Assess this cell for malaria.
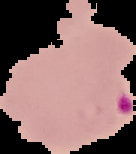
It is parasitized.

Segmented cell region on a black background. From a thin blood smear. Image is 136×154 pixels.